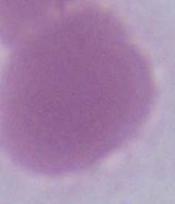

identification = erythrocyte
modality = photomicrograph
magnification = 1000x